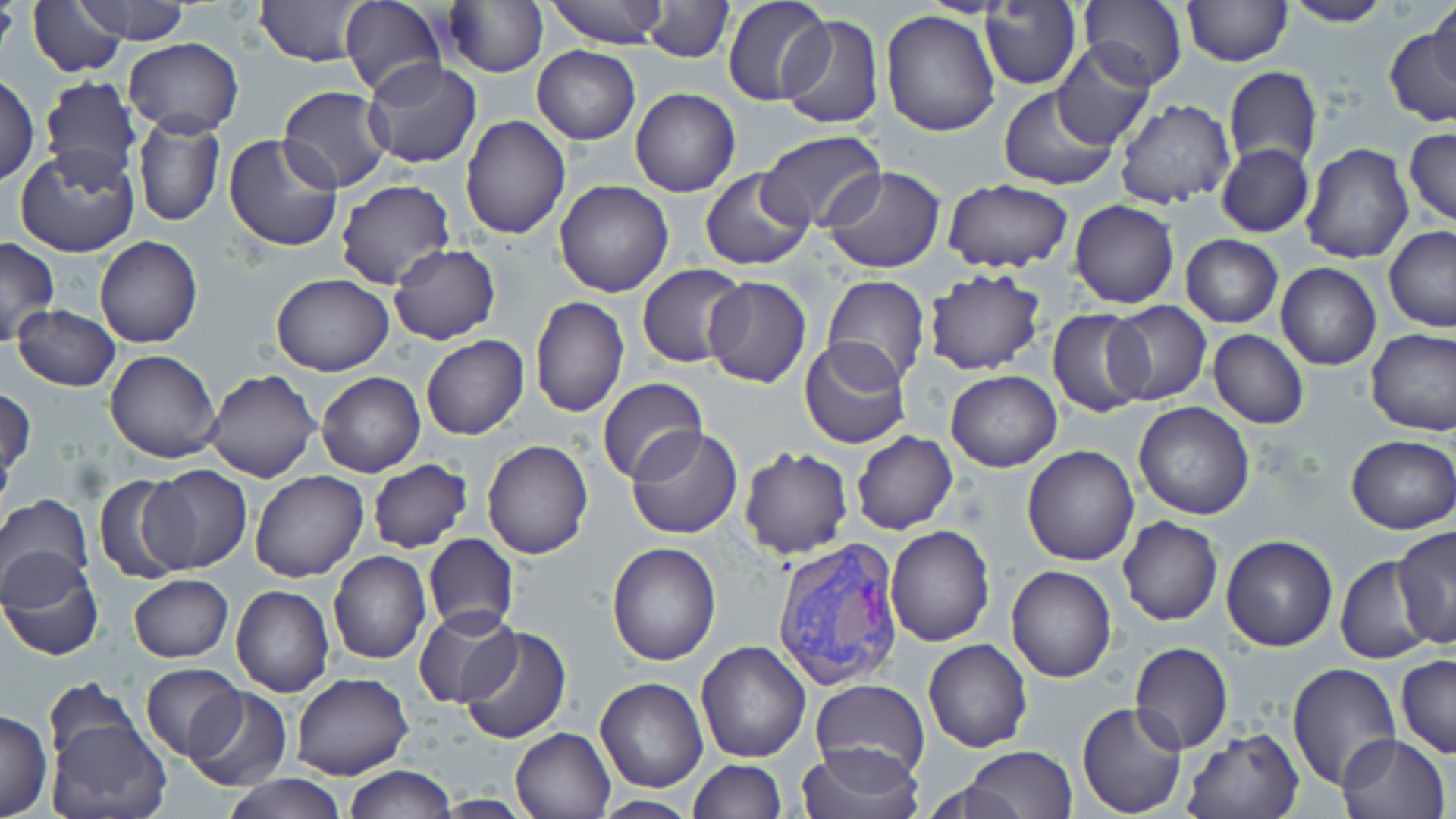

Summary:
  - Coordinate format: approximate bounding boxes as (x1, y1, x2, y2) in pixels
  - Uninfected red blood cell locations: (26, 0, 132, 76), (78, 0, 193, 45), (254, 0, 371, 66), (339, 0, 447, 99), (439, 0, 547, 77), (543, 0, 667, 48), (641, 0, 734, 61), (722, 0, 831, 105), (1181, 0, 1291, 66), (1427, 0, 1456, 94), (1079, 1, 1189, 90), (1278, 1, 1394, 28), (0, 2, 19, 67), (979, 3, 1082, 89), (881, 9, 1001, 137), (778, 13, 885, 130), (1384, 22, 1456, 128), (123, 36, 243, 137), (1049, 43, 1155, 149), (533, 45, 640, 144), (364, 61, 482, 169), (1223, 68, 1322, 168), (0, 74, 39, 184), (40, 76, 142, 185), (997, 85, 1119, 192), (278, 87, 392, 193), (631, 88, 741, 196), (1113, 99, 1237, 208), (132, 113, 225, 228), (460, 117, 570, 239), (1403, 127, 1456, 228), (756, 131, 888, 234), (223, 133, 343, 253), (1299, 143, 1415, 264), (1215, 144, 1314, 238), (15, 145, 141, 257), (821, 166, 945, 275), (700, 167, 814, 270), (335, 178, 455, 291), (940, 180, 1072, 272), (554, 181, 674, 297), (1070, 200, 1178, 309), (1383, 225, 1456, 331), (1181, 234, 1283, 328), (0, 235, 59, 346), (94, 237, 203, 349), (386, 244, 501, 345), (1276, 262, 1382, 371), (637, 263, 747, 367), (922, 269, 1047, 377), (270, 274, 395, 376), (701, 275, 812, 389), (820, 275, 932, 387), (529, 296, 629, 419), (1105, 301, 1212, 405), (14, 305, 121, 391), (1047, 311, 1151, 416), (1366, 327, 1456, 436), (1207, 329, 1309, 429), (421, 335, 529, 439), (799, 338, 911, 450), (103, 350, 222, 463), (204, 369, 320, 482), (945, 371, 1063, 472), (316, 372, 425, 477), (596, 378, 709, 485), (1, 385, 36, 484), (1133, 400, 1255, 520), (628, 427, 743, 540), (852, 431, 958, 534), (1346, 434, 1456, 534), (483, 439, 594, 559), (1022, 445, 1140, 565), (738, 448, 854, 559), (365, 460, 473, 554), (141, 464, 252, 575), (249, 470, 370, 582), (93, 473, 194, 587), (0, 494, 94, 603), (1118, 516, 1222, 626), (885, 524, 995, 646), (1393, 526, 1456, 649), (423, 534, 517, 636), (1221, 535, 1338, 653), (606, 542, 721, 665), (328, 550, 431, 665), (1, 551, 105, 661), (1334, 557, 1435, 665), (1006, 565, 1116, 682), (127, 574, 234, 663), (231, 585, 335, 698), (414, 608, 522, 708), (456, 625, 571, 745), (923, 639, 1032, 753), (695, 641, 811, 763), (1129, 642, 1234, 753), (1396, 653, 1456, 759), (1285, 662, 1400, 792), (140, 663, 242, 760), (290, 673, 414, 781), (594, 677, 708, 793), (42, 678, 147, 777), (809, 679, 931, 784), (183, 685, 291, 792), (1077, 701, 1188, 817), (0, 708, 53, 819), (47, 712, 171, 817), (511, 728, 616, 817), (1179, 728, 1304, 819), (1336, 733, 1453, 819), (796, 743, 925, 819), (960, 747, 1078, 819), (687, 759, 786, 818), (345, 766, 456, 818), (221, 775, 348, 819)
  - Plasmodium vivax-infected red blood cell locations: (771, 538, 905, 692)
  - Slide-level diagnosis: Plasmodium vivax
  - Modality: light microscopy
  - Field of view: single
  - Stain: May-Grünwald-Giemsa
  - Magnification: 1000x
  - Preparation: thin blood smear
  - Image size: 1456×819 pixels